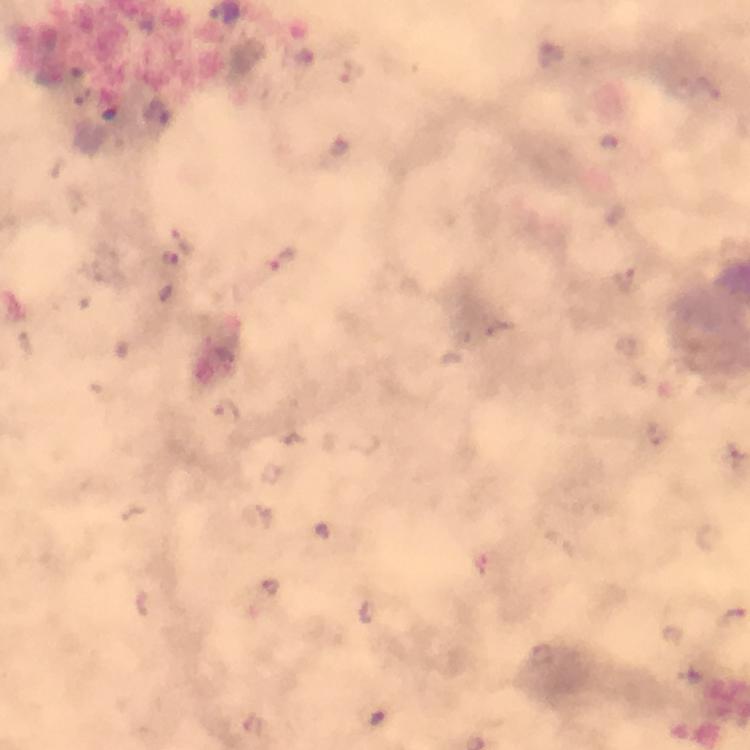 Approximate centers as [x, y] in pixels. Malaria parasite locations: [551, 54], [183, 240], [171, 257], [281, 261], [624, 274], [228, 410], [656, 432], [324, 531], [270, 587], [733, 619], [543, 653], [377, 718], [254, 728]. 100x magnification. Immersion oil was used. Image is 750×750 pixels. A crop from one field of view. Smartphone photograph taken through a microscope. Giemsa stain. Thick smear. From a diagnostic examination for malaria.